Describe the morphology of the red blood cells.
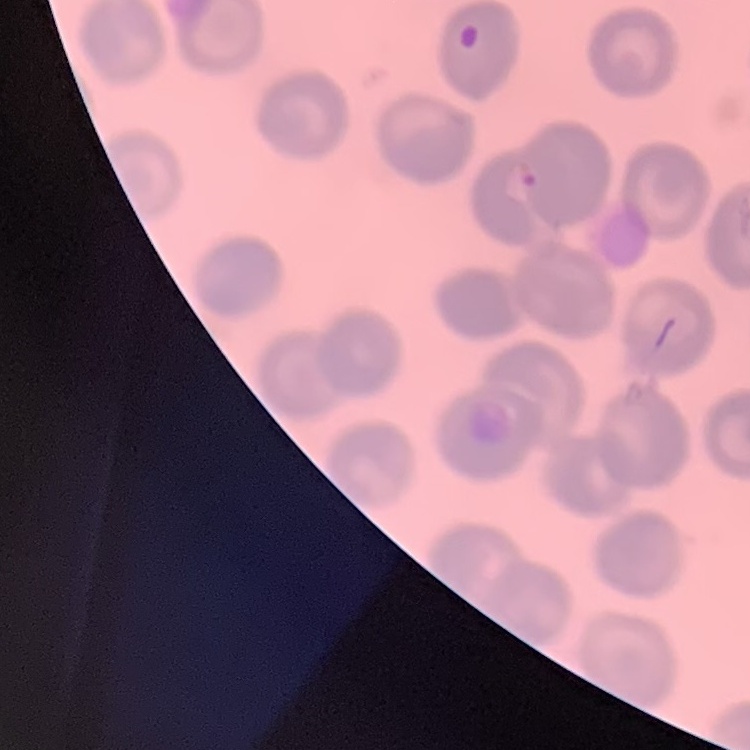

No rouleaux formation.

{
  "image_type": "square crop of a larger photomicrograph",
  "preparation": "thin peripheral smear",
  "stain": "Field's or Giemsa"
}